Give the position of every leukocyte visible.
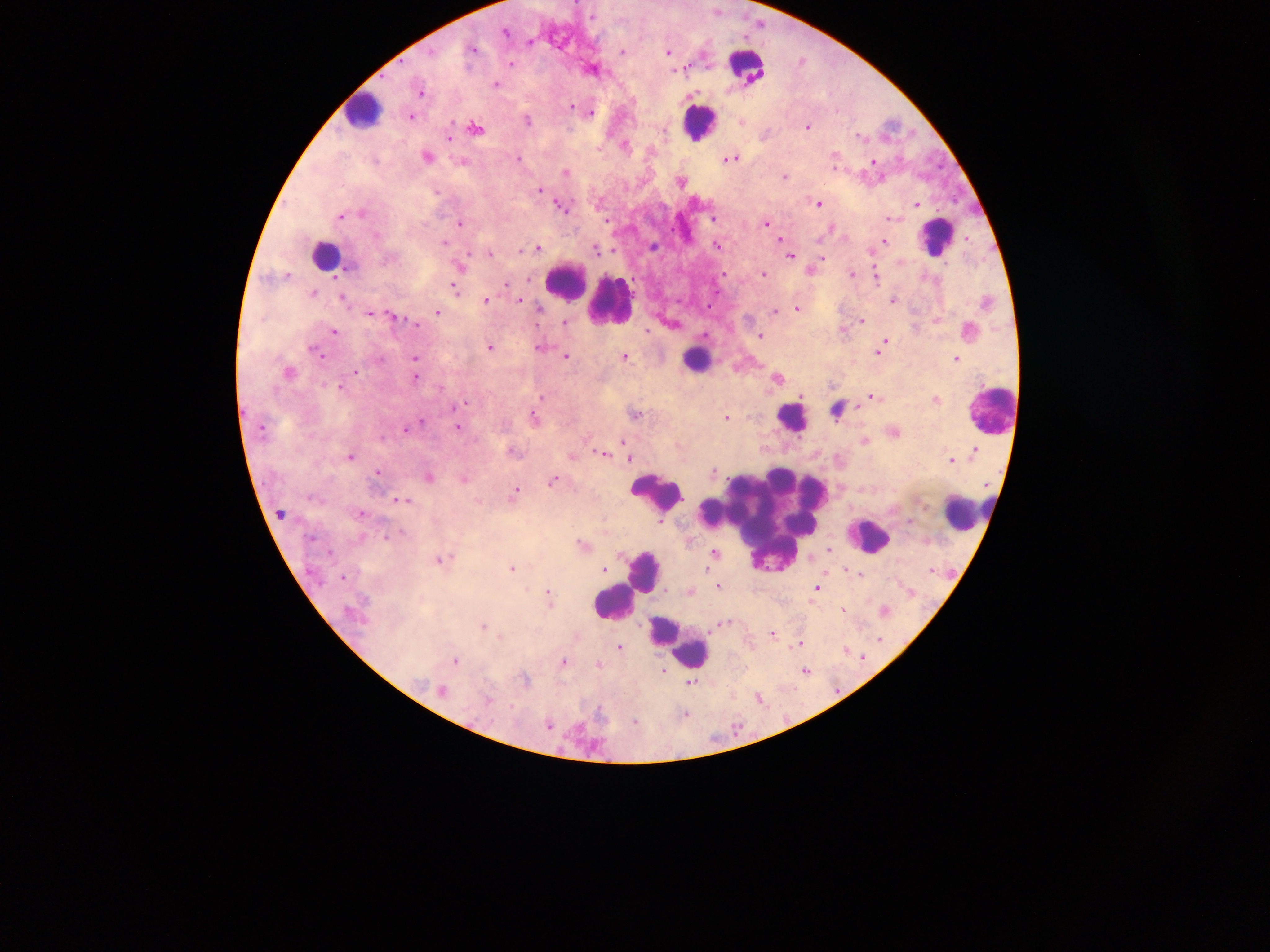

Approximate centers as (x, y) in pixels.
Leukocytes: (747, 69), (364, 112), (699, 124), (936, 238), (325, 255), (566, 282), (611, 303), (696, 361), (836, 410), (991, 413), (792, 420), (657, 492), (962, 517), (765, 524), (869, 538), (646, 572), (613, 603), (678, 640).

field_of_view: single
image_size: 1270×952 pixels
malaria_parasite_locations: 'approximate centers as (x, y) in pixels: (718, 12), (506, 34), (746, 38), (474, 51), (622, 52), (668, 52), (512, 65), (686, 70), (497, 86), (422, 93), (572, 107), (591, 115), (413, 118), (742, 122), (528, 123), (808, 128), (477, 129), (449, 139), (427, 158), (519, 160), (731, 160), (874, 162), (566, 174), (785, 177), (682, 183), (541, 191), (436, 192), (818, 204), (917, 206), (561, 207), (363, 215), (341, 218), (714, 218), (888, 219), (767, 224), (460, 225), (781, 241), (885, 242), (445, 244), (717, 247), (539, 249), (597, 250), (491, 256), (790, 257), (763, 276), (852, 276), (529, 280), (506, 285), (455, 289), (315, 295), (345, 299), (520, 300), (486, 302), (894, 302), (540, 311), (798, 311), (776, 313), (437, 314), (370, 315), (393, 317), (862, 322), (565, 323), (415, 324), (335, 332), (761, 337), (491, 349), (540, 349), (881, 349), (313, 352), (319, 355), (566, 357), (415, 359), (625, 359), (956, 359), (356, 374), (416, 378), (778, 380), (340, 387), (543, 397), (873, 399), (936, 400), (463, 404), (636, 415), (535, 418), (728, 419), (422, 424), (458, 427), (406, 430), (865, 443), (624, 444), (975, 452), (515, 454), (604, 455), (573, 457), (351, 458), (629, 460), (952, 461), (378, 473), (715, 473), (429, 479), (466, 480), (554, 481), (515, 494), (404, 501), (362, 514), (282, 515), (661, 522), (311, 541), (583, 546), (829, 550), (715, 554), (453, 560), (440, 561), (513, 570), (605, 570), (846, 571), (934, 571), (343, 579), (719, 587), (818, 589), (548, 593), (691, 593), (912, 594), (549, 602), (843, 610), (885, 613), (727, 624), (483, 628), (773, 635), (501, 637), (880, 641), (801, 644), (620, 648), (847, 653), (862, 658), (456, 662), (564, 663), (599, 666), (664, 672), (806, 672), (526, 682), (691, 683), (443, 693), (760, 700), (490, 701), (600, 714), (686, 717), (635, 723), (549, 727), (737, 728)'
country: Ghana
capture: mobile-phone photograph through a microscope
preparation: thick blood film